Give a bounding box for every malaria parasite, every leukocyte, and every artifact (stain precipitate or debris).
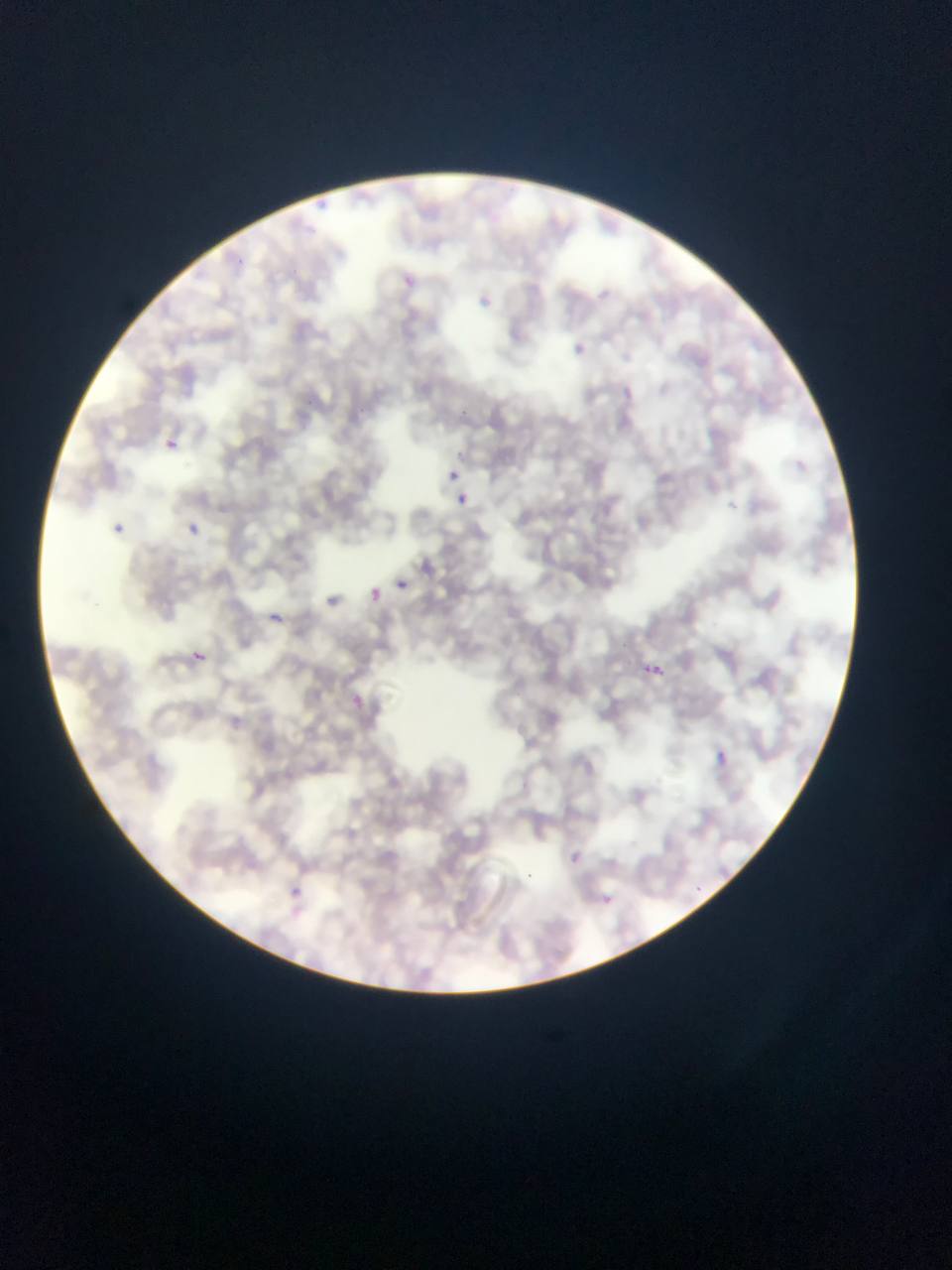

Approximate bounding boxes as left top right bottom in pixels.
Malaria parasites: 476 292 513 323; 566 335 594 366; 157 430 182 454; 445 467 461 484; 454 492 470 508; 181 520 204 542; 109 521 129 539; 384 569 421 597; 392 574 412 593; 367 585 386 605; 317 588 344 614; 258 604 290 634; 178 638 224 671; 183 645 210 670; 633 653 671 686; 339 687 373 717; 708 746 735 772; 276 882 319 925; 591 886 622 915.
No leukocytes observed.

Summary:
  - Country: Ghana
  - Preparation: thin blood film
  - Field of view: single
  - Capture: mobile-phone photograph through a microscope
  - Image size: 952×1270 pixels